Mark where leukocytes are.
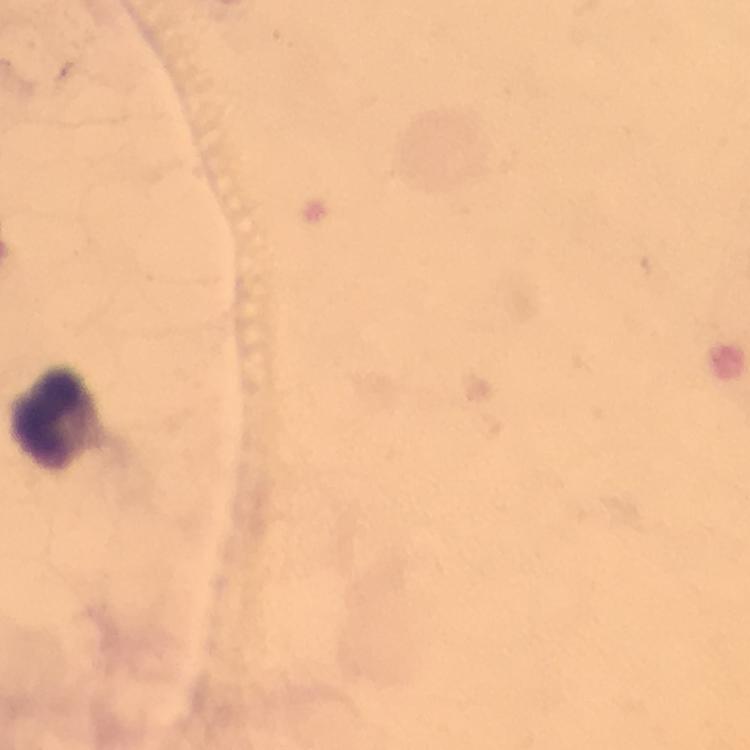
Approximate centers as {x, y} in pixels.
Leukocytes: {54, 412}.

Summary:
  - Magnification: 100x
  - Preparation: thick blood smear
  - Plasmodium parasites: none seen
  - Capture: smartphone photograph through a microscope
  - Image size: 750×750 pixels
  - Immersion oil: applied
  - Context: from a diagnostic examination for malaria
  - Cropped from: a single field of view
  - Stain: Giemsa